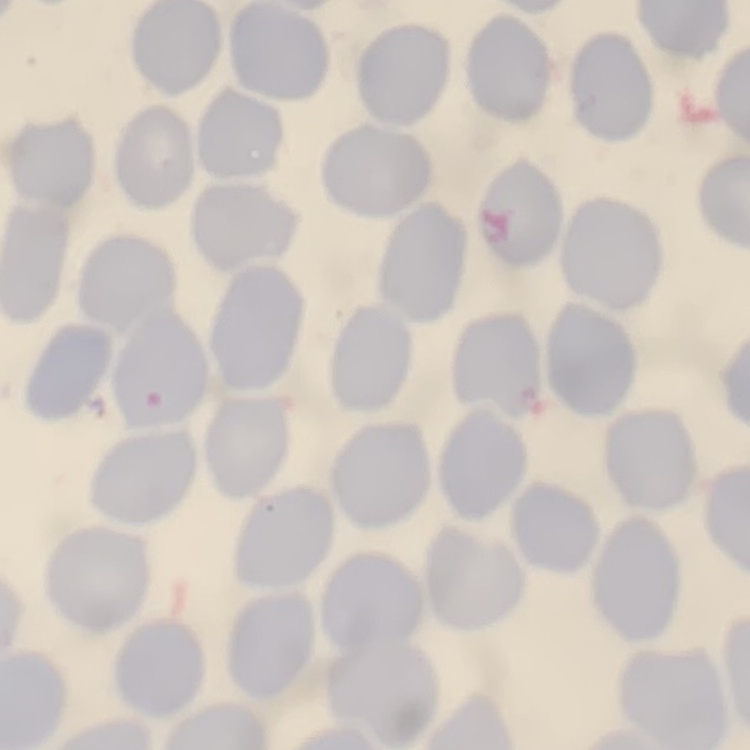

The erythrocytes show no rouleaux formation. Square crop of a larger photomicrograph. Thin blood film. Stained with either Field's or Giemsa.